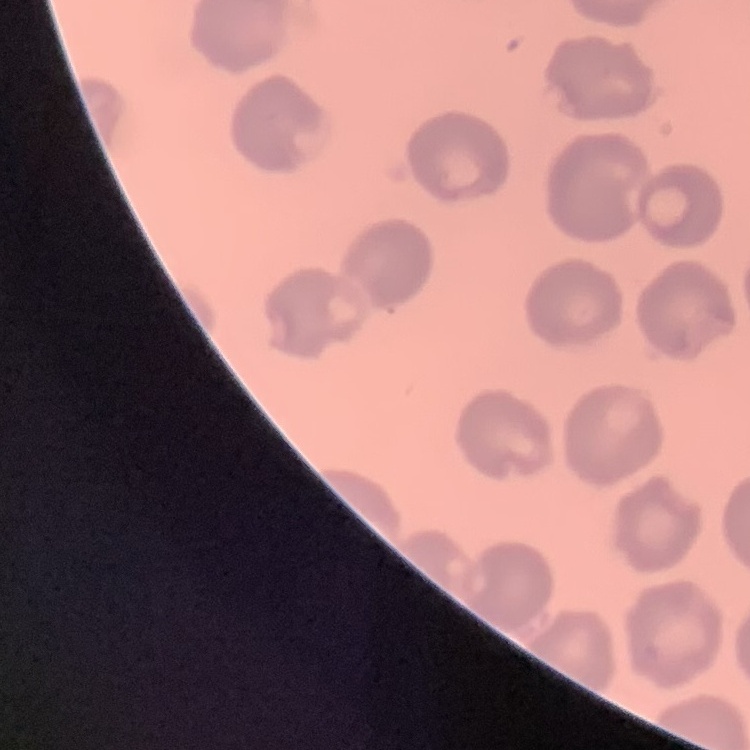 The red blood cells exhibit no rouleaux formation. Square crop of a larger photomicrograph. Field's or Giemsa stain. Thin blood film.